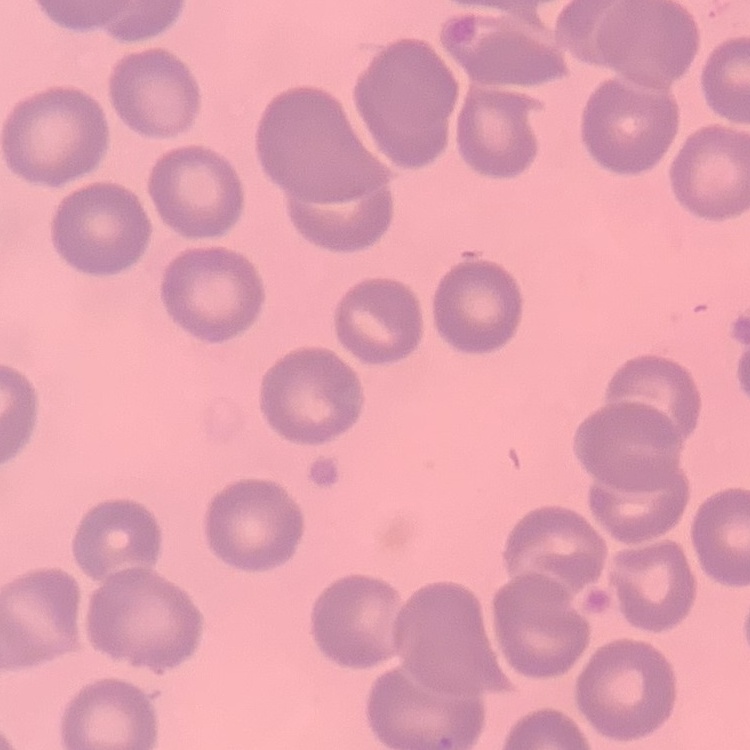
The erythrocytes exhibit no rouleaux formation. Thin blood smear. Stained with either Field's or Giemsa. One tile cut from a larger photomicrograph.